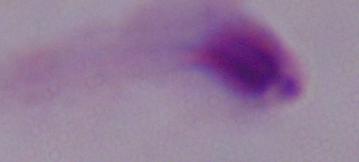

Summary:
  - Identification: trichomonad
  - Magnification: 1000x
  - Modality: micrograph